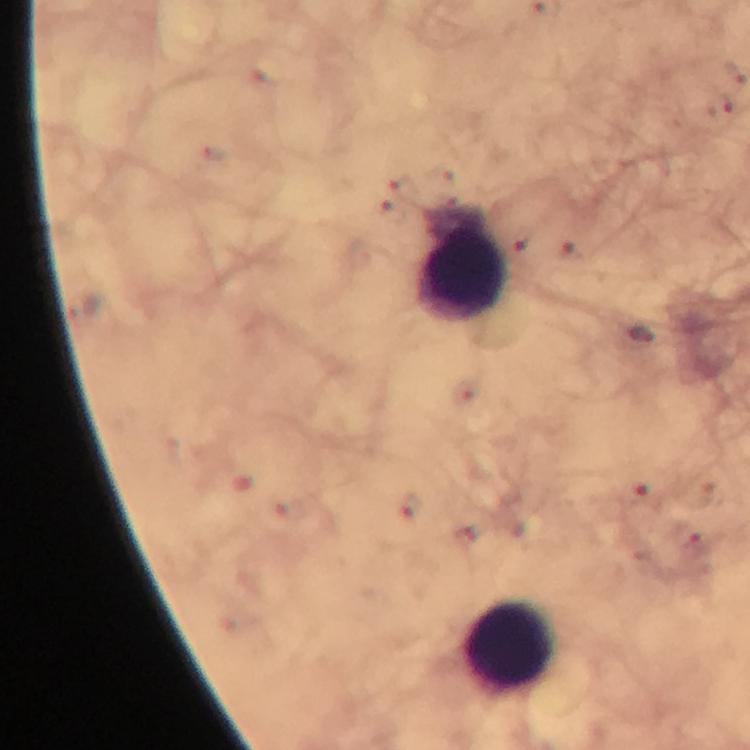
{
  "cropped_from": "a single field of view",
  "image_size": "750×750 pixels",
  "immersion_oil": "applied",
  "preparation": "thick smear",
  "leukocyte_locations": "approximate centers as (x, y) in pixels: (462, 267), (510, 644)",
  "plasmodium_parasite_locations": "approximate centers as (x, y) in pixels: (719, 106), (644, 336), (640, 492)",
  "context": "from a diagnostic examination for malaria",
  "capture": "smartphone camera through the microscope",
  "stain": "Giemsa",
  "magnification": "100x"
}